Outline each Plasmodium vivax-infected red blood cell.
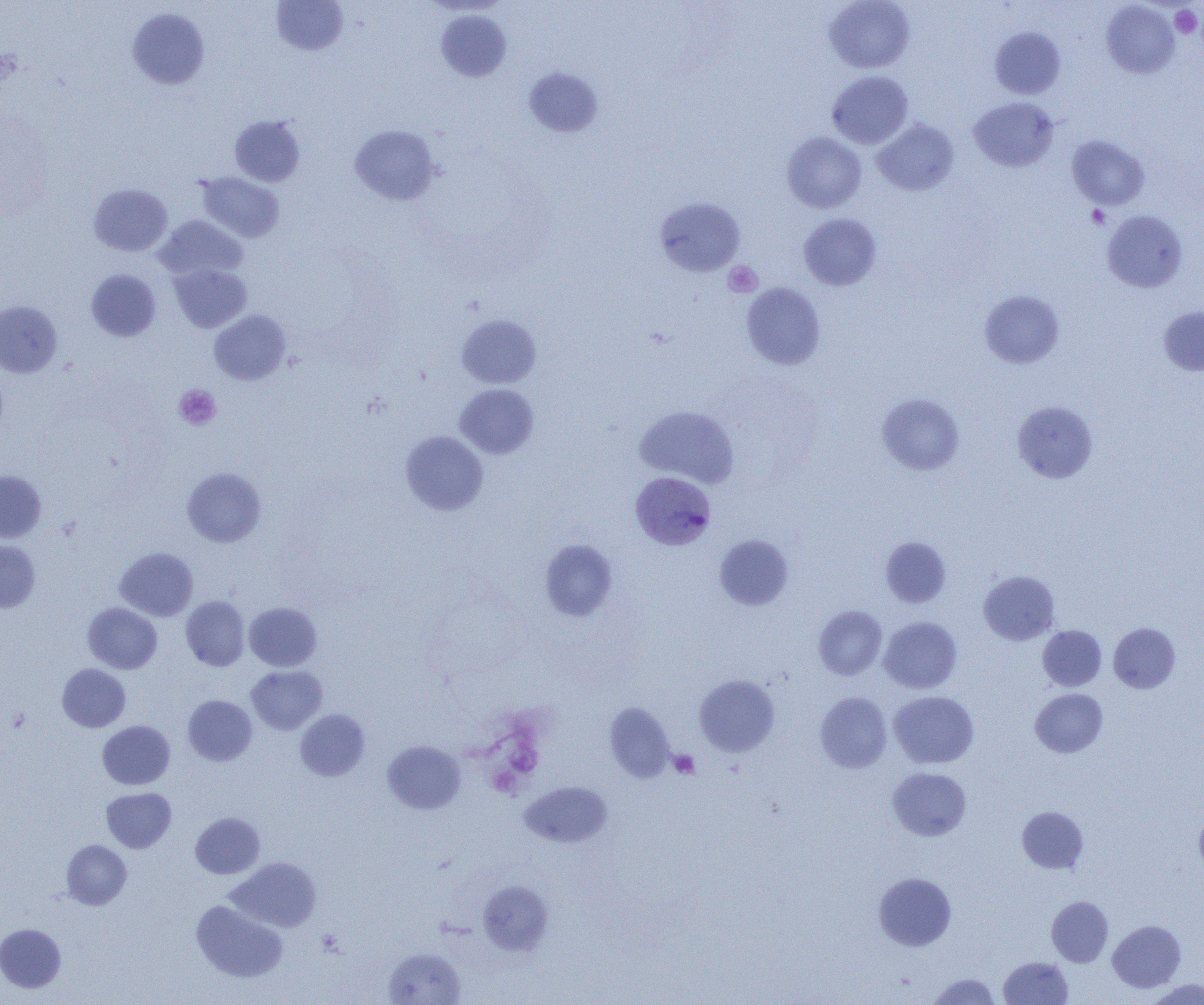
Approximate bounding boxes as named x1/y1/x2/y2 corners in pixels.
Plasmodium vivax-infected red blood cells: (x1=630, y1=471, x2=716, y2=550).

slide_level_diagnosis: Plasmodium vivax
modality: light microscopy
image_size: 1204×1005 pixels
magnification: 1000x
uninfected_red_blood_cell_locations: 'approximate bounding boxes as named x1/y1/x2/y2 corners in pixels: (x1=824, y1=0, x2=915, y2=73), (x1=271, y1=1, x2=348, y2=56), (x1=1101, y1=2, x2=1179, y2=79), (x1=127, y1=7, x2=210, y2=89), (x1=436, y1=10, x2=511, y2=82), (x1=989, y1=27, x2=1065, y2=99), (x1=525, y1=67, x2=604, y2=137), (x1=827, y1=71, x2=913, y2=148), (x1=969, y1=97, x2=1059, y2=172), (x1=229, y1=115, x2=305, y2=187), (x1=872, y1=118, x2=960, y2=196), (x1=349, y1=125, x2=442, y2=206), (x1=781, y1=132, x2=867, y2=213), (x1=1067, y1=135, x2=1149, y2=210), (x1=197, y1=172, x2=285, y2=243), (x1=88, y1=183, x2=172, y2=256), (x1=653, y1=197, x2=745, y2=277), (x1=1101, y1=210, x2=1187, y2=293), (x1=799, y1=213, x2=881, y2=291), (x1=155, y1=216, x2=248, y2=281), (x1=169, y1=264, x2=251, y2=332), (x1=86, y1=269, x2=160, y2=341), (x1=741, y1=283, x2=825, y2=370), (x1=980, y1=290, x2=1064, y2=369), (x1=0, y1=301, x2=62, y2=378), (x1=1159, y1=306, x2=1204, y2=376), (x1=209, y1=310, x2=291, y2=385), (x1=457, y1=315, x2=541, y2=388), (x1=455, y1=383, x2=539, y2=459), (x1=877, y1=393, x2=965, y2=475), (x1=1012, y1=401, x2=1098, y2=483), (x1=634, y1=405, x2=740, y2=488), (x1=400, y1=431, x2=488, y2=515), (x1=182, y1=467, x2=266, y2=547), (x1=0, y1=470, x2=46, y2=543), (x1=714, y1=534, x2=793, y2=610), (x1=881, y1=537, x2=951, y2=608), (x1=0, y1=540, x2=40, y2=612), (x1=538, y1=540, x2=617, y2=621), (x1=114, y1=547, x2=198, y2=621), (x1=979, y1=571, x2=1059, y2=645), (x1=181, y1=596, x2=249, y2=671), (x1=83, y1=602, x2=162, y2=674), (x1=244, y1=602, x2=322, y2=671), (x1=813, y1=605, x2=887, y2=680), (x1=879, y1=617, x2=962, y2=693), (x1=1108, y1=622, x2=1180, y2=693), (x1=1038, y1=625, x2=1106, y2=691), (x1=57, y1=664, x2=130, y2=732), (x1=246, y1=665, x2=327, y2=735), (x1=694, y1=674, x2=780, y2=756), (x1=1030, y1=688, x2=1108, y2=757), (x1=889, y1=691, x2=979, y2=768), (x1=815, y1=692, x2=892, y2=773), (x1=182, y1=695, x2=257, y2=766), (x1=605, y1=702, x2=675, y2=782), (x1=295, y1=709, x2=370, y2=781), (x1=97, y1=721, x2=175, y2=789), (x1=382, y1=741, x2=466, y2=814), (x1=888, y1=767, x2=971, y2=840), (x1=520, y1=782, x2=612, y2=848), (x1=101, y1=787, x2=176, y2=852), (x1=1017, y1=807, x2=1088, y2=873), (x1=1194, y1=811, x2=1204, y2=875), (x1=190, y1=812, x2=265, y2=878), (x1=61, y1=840, x2=131, y2=909), (x1=227, y1=857, x2=321, y2=932), (x1=873, y1=873, x2=956, y2=952), (x1=478, y1=880, x2=553, y2=955), (x1=1047, y1=896, x2=1113, y2=967), (x1=191, y1=900, x2=287, y2=982), (x1=1107, y1=920, x2=1185, y2=992), (x1=0, y1=924, x2=66, y2=993), (x1=384, y1=947, x2=465, y2=1005), (x1=999, y1=956, x2=1073, y2=1004), (x1=926, y1=973, x2=1001, y2=1004), (x1=1145, y1=979, x2=1204, y2=1004)'
preparation: thin blood film
platelet_locations: 'approximate bounding boxes as named x1/y1/x2/y2 corners in pixels: (x1=1170, y1=5, x2=1202, y2=38), (x1=1, y1=48, x2=23, y2=86), (x1=1086, y1=205, x2=1110, y2=229), (x1=723, y1=261, x2=763, y2=297), (x1=174, y1=384, x2=220, y2=430), (x1=669, y1=750, x2=699, y2=779)'
field_of_view: single